Report the malaria status of this cell.
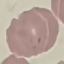
It is parasitized.

Photographed with a smartphone camera at the microscope eyepiece. Thin blood smear. Giemsa stain. Cell patch, automatically extracted from a larger field of view and resized to 64 × 64 pixels.